Locate cells.
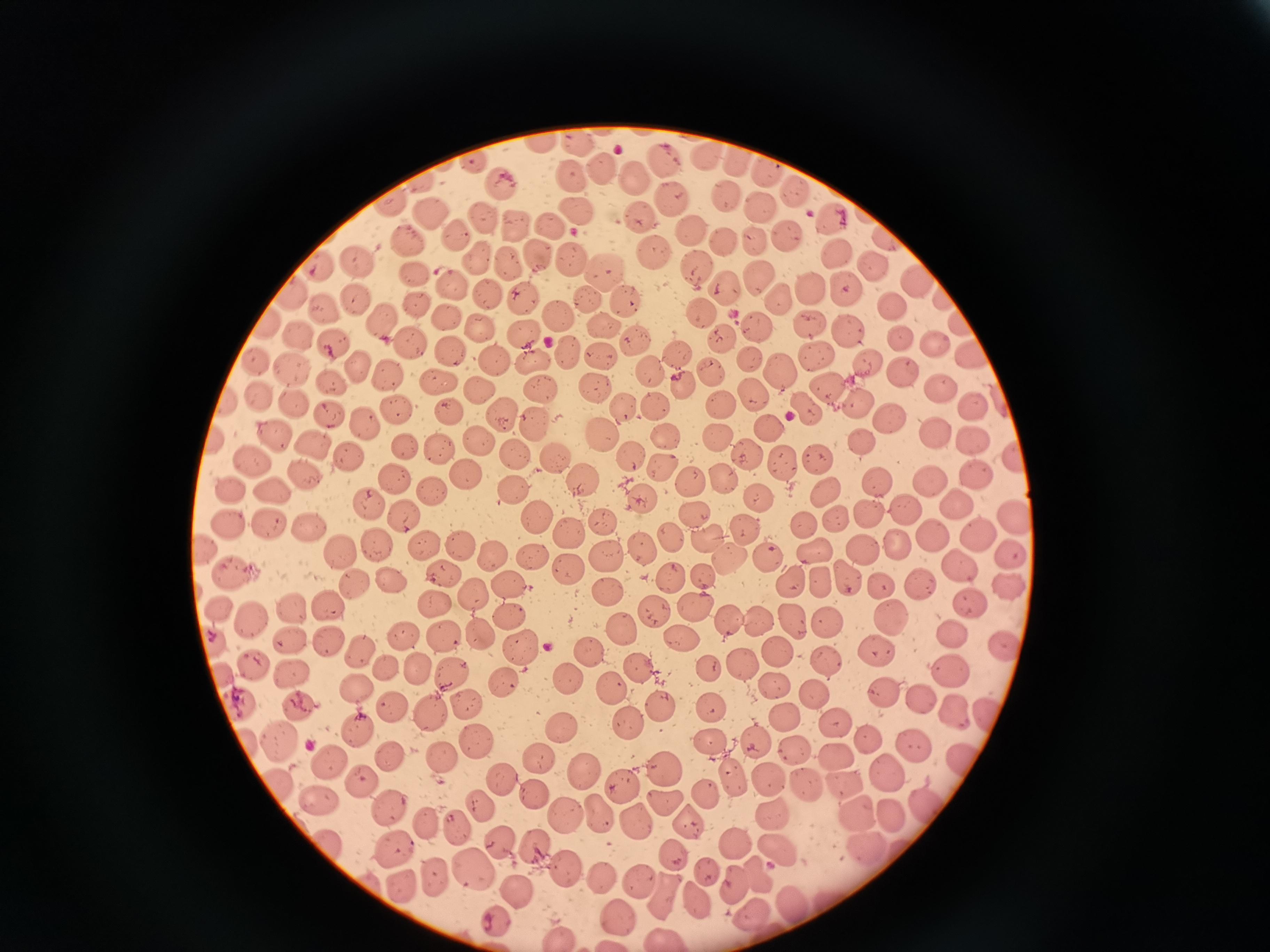
Approximate centers as {x, y} in pixels.
Cells: {540, 144}, {582, 144}, {713, 154}, {745, 159}, {662, 161}, {477, 165}, {768, 168}, {598, 171}, {633, 175}, {572, 177}, {420, 184}, {500, 186}, {724, 196}, {670, 199}, {395, 204}, {759, 205}, {574, 210}, {432, 213}, {640, 213}, {481, 219}, {513, 223}, {551, 225}, {690, 231}, {457, 239}, {785, 239}, {724, 241}, {408, 242}, {754, 242}, {649, 249}, {838, 251}, {535, 252}, {566, 255}, {355, 258}, {475, 259}, {321, 263}, {509, 263}, {696, 267}, {606, 273}, {760, 279}, {915, 279}, {452, 283}, {810, 283}, {725, 286}, {845, 286}, {484, 288}, {297, 293}, {522, 294}, {941, 296}, {587, 298}, {781, 299}, {623, 300}, {357, 302}, {415, 303}, {893, 306}, {324, 310}, {555, 310}, {448, 314}, {386, 315}, {702, 315}, {953, 318}, {809, 321}, {483, 324}, {758, 324}, {601, 325}, {849, 327}, {525, 332}, {723, 336}, {300, 337}, {903, 337}, {934, 340}, {412, 343}, {332, 345}, {452, 349}, {566, 350}, {679, 352}, {813, 353}, {970, 353}, {534, 357}, {601, 357}, {748, 357}, {493, 358}, {257, 359}, {865, 362}, {361, 363}, {711, 365}, {292, 368}, {653, 369}, {389, 371}, {783, 372}, {906, 372}, {436, 378}, {334, 382}, {684, 382}, {942, 384}, {826, 386}, {544, 387}, {593, 387}, {481, 389}, {750, 393}, {259, 397}, {228, 399}, {724, 400}, {858, 400}, {295, 404}, {626, 404}, {658, 405}, {973, 407}, {398, 409}, {329, 410}, {806, 410}, {448, 411}, {887, 414}, {503, 416}, {368, 421}, {539, 424}, {768, 428}, {603, 429}, {935, 433}, {271, 434}, {718, 435}, {478, 436}, {665, 436}, {971, 437}, {220, 439}, {863, 439}, {316, 443}, {408, 448}, {441, 449}, {517, 454}, {747, 454}, {822, 455}, {1017, 455}, {348, 458}, {631, 458}, {558, 459}, {255, 461}, {784, 462}, {661, 463}, {975, 470}, {464, 471}, {304, 477}, {397, 477}, {721, 478}, {932, 479}, {876, 480}, {691, 481}, {584, 484}, {234, 487}, {513, 487}, {433, 488}, {826, 488}, {276, 489}, {756, 494}, {643, 495}, {370, 499}, {954, 500}, {908, 508}, {873, 512}, {404, 514}, {695, 514}, {841, 514}, {1017, 514}, {534, 517}, {227, 518}, {603, 520}, {806, 521}, {271, 525}, {312, 526}, {748, 530}, {567, 531}, {934, 531}, {975, 532}, {673, 537}, {425, 540}, {210, 544}, {376, 544}, {461, 544}, {860, 546}, {896, 546}, {816, 547}, {642, 548}, {339, 549}, {1011, 549}, {494, 550}, {730, 553}, {768, 553}, {531, 554}, {609, 554}, {959, 558}, {572, 566}, {233, 570}, {444, 571}, {702, 575}, {392, 576}, {673, 577}, {784, 577}, {843, 577}, {512, 580}, {822, 580}, {356, 583}, {882, 583}, {1006, 584}, {918, 585}, {610, 591}, {331, 604}, {696, 604}, {969, 604}, {297, 606}, {512, 608}, {222, 609}, {654, 609}, {889, 613}, {253, 617}, {759, 617}, {729, 618}, {827, 618}, {792, 620}, {478, 631}, {404, 632}, {683, 633}, {625, 634}, {956, 634}, {328, 635}, {216, 636}, {292, 637}, {1001, 645}, {522, 646}, {879, 648}, {588, 650}, {365, 651}, {780, 651}, {828, 659}, {419, 663}, {743, 663}, {255, 664}, {389, 666}, {642, 666}, {947, 668}, {294, 670}, {709, 670}, {452, 671}, {222, 672}, {566, 677}, {502, 679}, {774, 684}, {359, 686}, {611, 688}, {814, 691}, {884, 692}, {919, 698}, {243, 699}, {300, 702}, {658, 704}, {714, 705}, {391, 706}, {470, 706}, {951, 711}, {989, 711}, {433, 715}, {785, 715}, {624, 722}, {834, 722}, {564, 725}, {359, 730}, {276, 738}, {871, 738}, {712, 740}, {914, 740}, {754, 742}, {481, 748}, {791, 749}, {387, 752}, {440, 753}, {833, 754}, {539, 758}, {332, 760}, {965, 761}, {665, 767}, {584, 771}, {890, 771}, {367, 777}, {769, 777}, {735, 781}, {501, 782}, {620, 782}, {846, 782}, {804, 783}, {538, 788}, {315, 795}, {708, 795}, {932, 799}, {481, 800}, {663, 801}, {391, 804}, {602, 812}, {772, 815}, {861, 816}, {895, 816}, {567, 817}, {640, 822}, {428, 823}, {691, 825}, {459, 826}, {499, 836}, {731, 838}, {394, 842}, {536, 844}, {781, 845}, {861, 845}, {677, 856}, {709, 869}, {472, 870}, {566, 870}, {759, 874}, {734, 879}, {642, 880}, {438, 881}, {606, 881}, {520, 888}, {401, 889}, {668, 893}, {698, 895}, {794, 898}, {754, 914}, {621, 917}, {496, 921}, {558, 934}, {665, 937}.

Summary:
  - Stain: Giemsa
  - Image size: 1270×952 pixels
  - Capture: smartphone through the microscope eyepiece
  - Field of view: single
  - Preparation: thin blood film